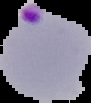

Summary:
  - Image type: cell region segmented out of the field of view; surrounding area masked to black
  - Malaria status: parasitized
  - Image size: 91×103 pixels
  - Preparation: thin blood film